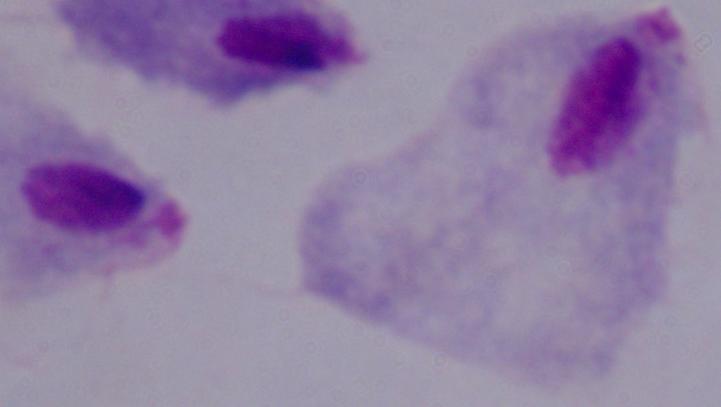 1000x magnification. Photomicrograph. A trichomonad is seen.